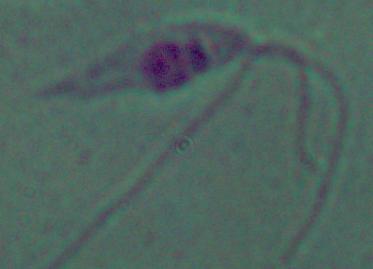

identification: Leishmania
modality: micrograph
magnification: 1000x